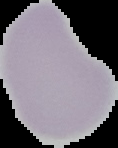
preparation = thin blood smear
result = no Plasmodium parasites seen
image type = segmented cell region on a black background
image size = 118×148 pixels